Classify this cell by malaria status.
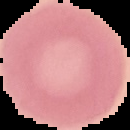

It is uninfected.

Summary:
  - Preparation: thin blood film
  - Image size: 130×130 pixels
  - Image type: cell region segmented out of the field of view; surrounding area masked to black